State which parasite is depicted.
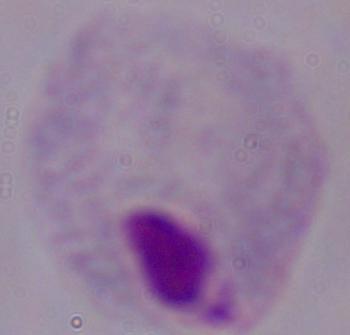

This is a trichomonad.

Summary:
  - Modality: photomicrograph
  - Magnification: 1000x